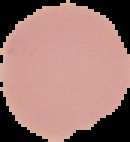

preparation = thin blood smear
image type = cell region segmented out of the field of view; surrounding area masked to black
malaria status = uninfected
image size = 130×142 pixels